Assess the morphology of the red blood cells.
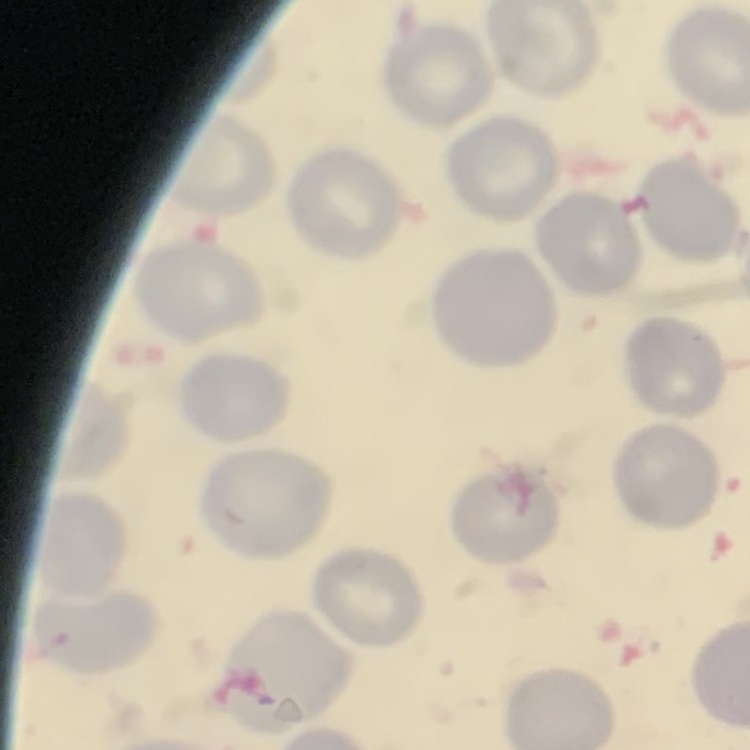
No rouleaux formation.

image type = one tile cut from a larger photomicrograph
preparation = thin blood smear
stain = Field's or Giemsa